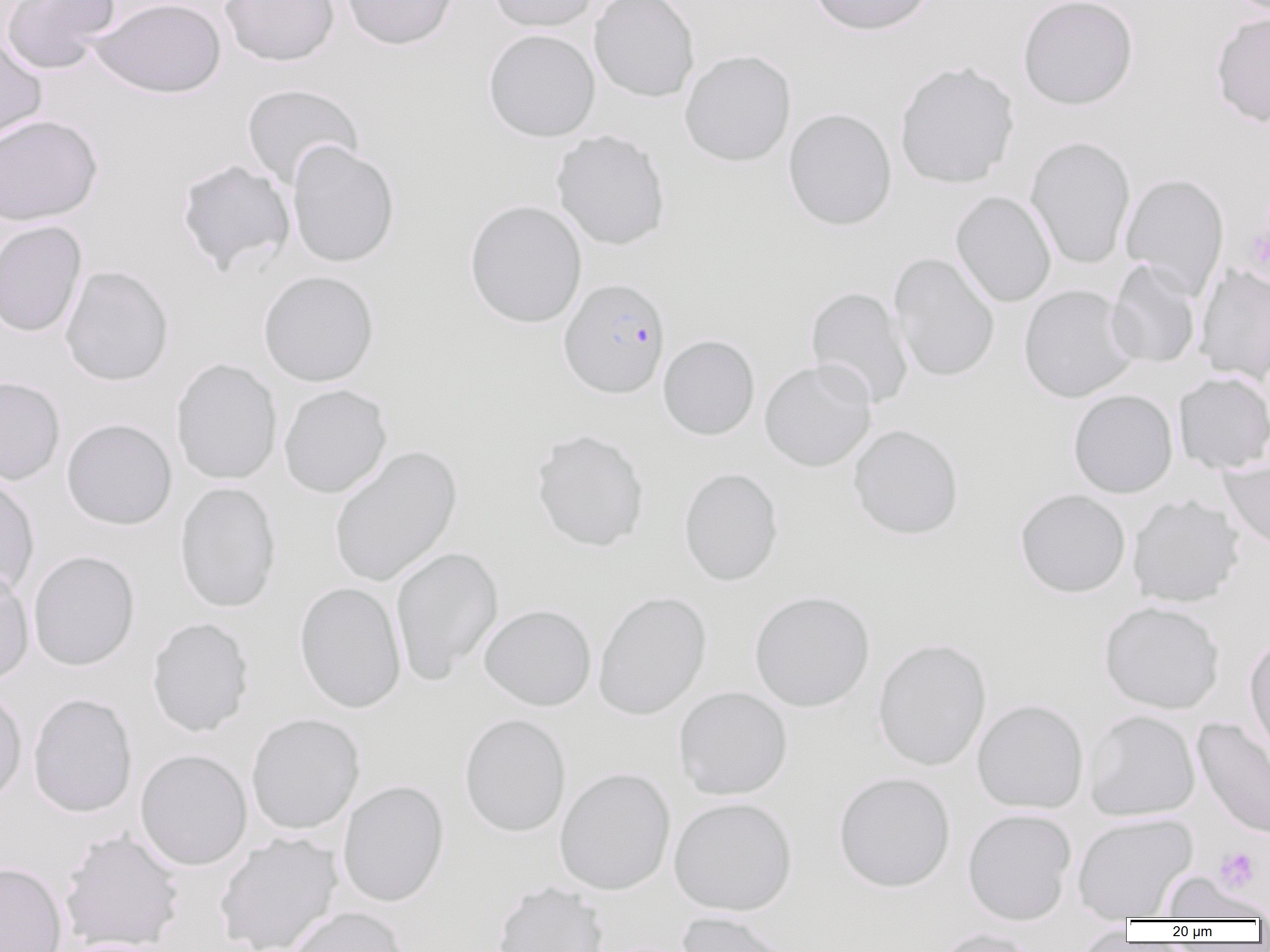

Summary:
  - Coordinate format: approximate bounding boxes as [x1, y1, x2, y2] in pixels
  - Plasmodium falciparum-infected red blood cell locations: [559, 277, 670, 399]
  - Platelet locations: [1242, 203, 1270, 283], [1214, 847, 1260, 892]
  - Uninfected red blood cell locations: [0, 0, 120, 75], [91, 0, 227, 99], [219, 0, 339, 66], [341, 0, 458, 50], [487, 0, 599, 33], [589, 0, 700, 102], [809, 0, 937, 36], [1017, 0, 1138, 110], [1210, 11, 1270, 128], [483, 29, 600, 142], [0, 36, 47, 145], [679, 50, 796, 166], [894, 61, 1020, 189], [241, 83, 364, 190], [783, 108, 897, 231], [0, 114, 102, 225], [551, 130, 671, 251], [1025, 135, 1136, 270], [287, 141, 400, 268], [176, 159, 296, 275], [1120, 173, 1230, 298], [950, 191, 1056, 307], [464, 200, 587, 329], [0, 220, 87, 338], [889, 252, 1000, 383], [1105, 259, 1202, 369], [1194, 264, 1270, 385], [60, 265, 174, 386], [258, 270, 379, 387], [805, 285, 914, 409], [1018, 285, 1139, 403], [658, 334, 759, 441], [171, 358, 282, 485], [759, 359, 877, 472], [1173, 372, 1270, 473], [0, 376, 65, 485], [278, 384, 392, 498], [1068, 389, 1178, 498], [61, 418, 177, 530], [848, 424, 964, 540], [530, 428, 650, 552], [329, 445, 462, 588], [1219, 457, 1270, 555], [679, 467, 783, 586], [0, 473, 40, 599], [174, 482, 282, 612], [1014, 488, 1131, 597], [1127, 494, 1244, 608], [390, 546, 504, 684], [28, 550, 140, 671], [0, 565, 34, 686], [294, 581, 407, 713], [593, 590, 712, 720], [749, 591, 875, 712], [1099, 600, 1225, 714], [478, 604, 597, 711], [146, 617, 254, 737], [1243, 633, 1270, 757], [872, 637, 992, 771], [0, 684, 27, 808], [673, 686, 793, 800], [28, 693, 137, 817], [971, 699, 1089, 814], [1083, 709, 1201, 822], [245, 713, 365, 835], [459, 713, 571, 838], [1192, 718, 1270, 839], [135, 749, 252, 871], [554, 767, 676, 895], [833, 772, 956, 892], [337, 780, 449, 907], [668, 796, 797, 916], [962, 808, 1077, 925], [1072, 813, 1197, 920], [59, 828, 186, 951], [214, 831, 344, 952], [0, 861, 68, 952], [1162, 871, 1268, 921], [491, 881, 609, 952], [287, 906, 410, 952], [676, 911, 795, 952], [1074, 925, 1136, 951], [930, 927, 1039, 952], [58, 937, 181, 952]
  - Slide-level diagnosis: Plasmodium falciparum
  - Preparation: thin blood smear
  - Image size: 1270×952 pixels
  - Magnification: 1000x
  - Modality: optical microscopy
  - Field of view: single